Give the extent of all uninfected red blood cells.
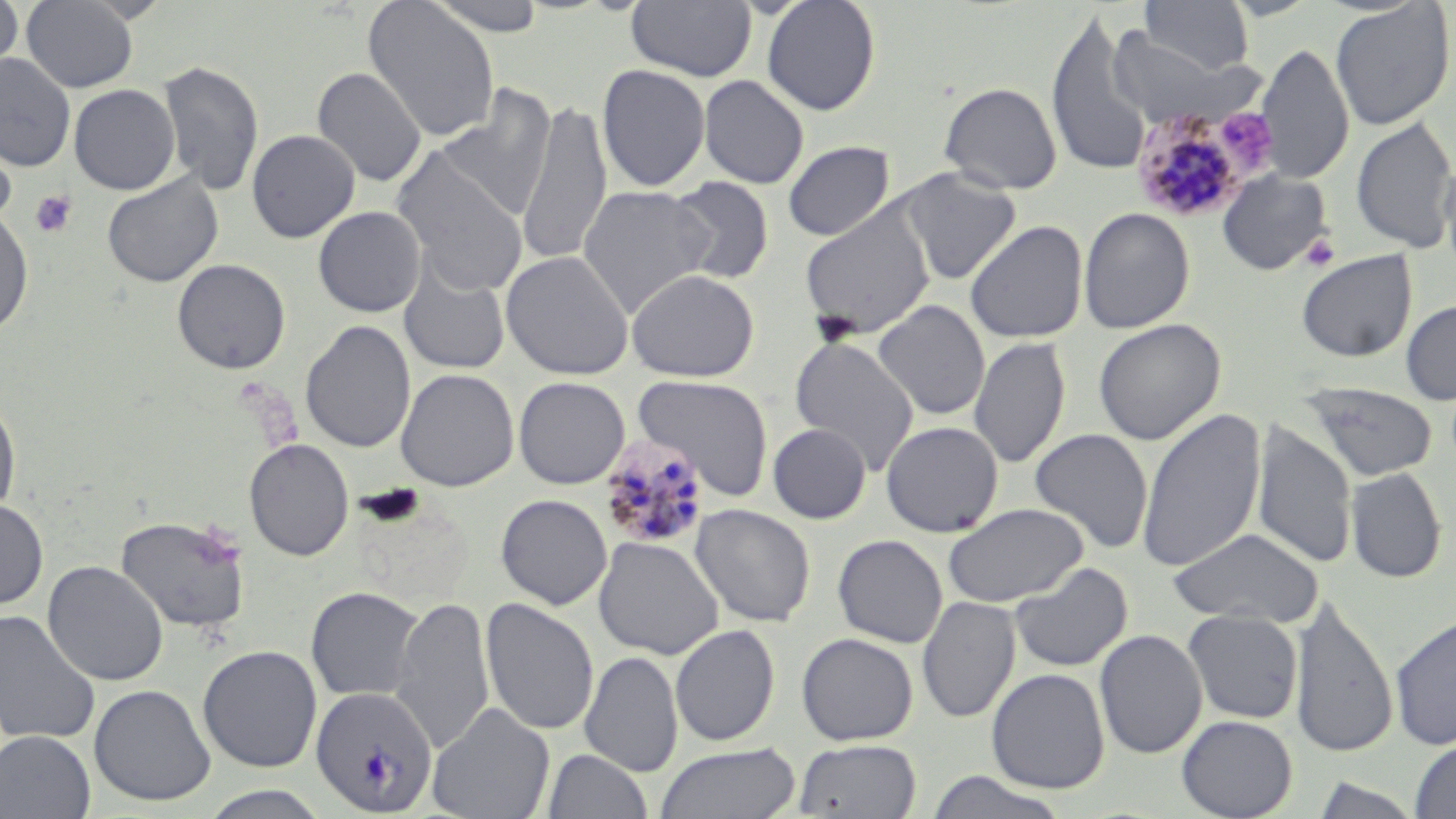
Approximate bounding boxes as (x1,y1)-(x2,y2) corner pairs in pixels.
Uninfected red blood cells (subset): (0,0)-(23,79), (21,0)-(139,92), (363,0)-(500,143), (425,0)-(550,37), (626,0)-(757,82), (761,0)-(882,116), (1140,0)-(1254,75), (1330,2)-(1454,130), (1046,11)-(1154,178), (1109,28)-(1244,127), (1256,42)-(1354,185), (0,53)-(76,172), (158,60)-(265,196), (597,63)-(710,192), (312,66)-(427,188), (698,75)-(809,189), (938,81)-(1061,195), (69,84)-(181,195), (435,84)-(558,224), (516,99)-(612,265), (1351,117)-(1456,253), (0,127)-(17,231), (246,129)-(360,243), (783,140)-(894,241), (391,147)-(528,296), (1438,154)-(1456,283), (896,167)-(1021,285), (1217,170)-(1334,275), (102,173)-(223,287), (665,177)-(774,285), (578,184)-(717,318), (313,206)-(426,317), (799,207)-(935,338), (1078,207)-(1195,333), (0,208)-(34,337), (964,220)-(1088,343), (1296,249)-(1417,362), (500,250)-(634,380), (171,259)-(290,374), (398,262)-(511,376), (626,269)-(760,382), (1400,298)-(1456,405), (872,300)-(990,421), (1093,318)-(1225,445), (300,320)-(416,453), (789,336)-(919,475), (968,336)-(1071,470), (395,368)-(519,492), (633,374)-(774,500), (1301,383)-(1438,481), (0,393)-(22,518), (1136,408)-(1266,573), (881,420)-(1003,537), (1252,422)-(1356,570), (768,423)-(871,523), (1030,428)-(1152,554), (244,438)-(354,561), (1345,467)-(1447,584), (495,494)-(612,610), (0,498)-(49,610), (943,503)-(1089,607), (690,504)-(816,627), (116,514)-(252,634), (1167,527)-(1324,627), (832,534)-(948,648), (593,536)-(724,659), (42,560)-(168,687), (1008,562)-(1133,673), (305,586)-(426,702), (390,596)-(495,753), (917,596)-(1021,724), (1289,596)-(1398,759), (480,598)-(599,735), (0,610)-(101,745), (1183,610)-(1303,724), (1390,613)-(1456,751), (670,624)-(780,747), (1095,629)-(1208,759), (796,632)-(919,746), (197,645)-(322,772), (579,650)-(683,778), (986,668)-(1110,793), (89,683)-(215,806), (427,703)-(555,819), (1177,715)-(1297,819), (0,730)-(96,818), (793,739)-(922,818), (1409,739)-(1456,819), (654,743)-(801,819), (542,748)-(652,819), (923,771)-(1072,819), (1312,776)-(1423,818), (198,785)-(335,818).

Platelet locations: (1215,109)-(1279,177), (31,190)-(77,238), (1300,233)-(1340,271). Plasmodium malariae-infected red blood cell locations (subset): (1130,103)-(1260,223), (598,435)-(710,550), (310,685)-(438,815). Slide-level diagnosis: Plasmodium malariae. May-Grünwald-Giemsa-stained preparation. Captured at 1000x magnification. Thin blood film. Single field of view. Light microscopy. Image is 1456×819 pixels.